Comment on the morphology of the red blood cells.
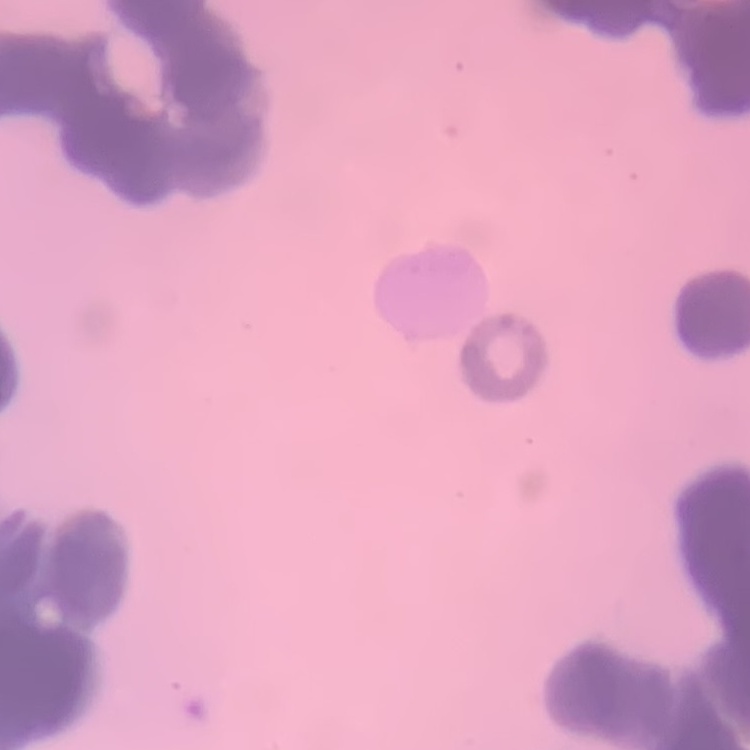

They show rouleaux formation.

Thin blood film. Square crop of a larger photomicrograph. Field's or Giemsa stain.